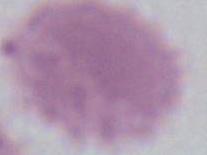
{
  "magnification": "1000x",
  "identification": "erythrocyte",
  "modality": "micrograph"
}